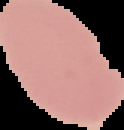
The area outside the segmented cell region is set to black. From a thin blood smear. Image is 124×130 pixels. Malaria status: uninfected.